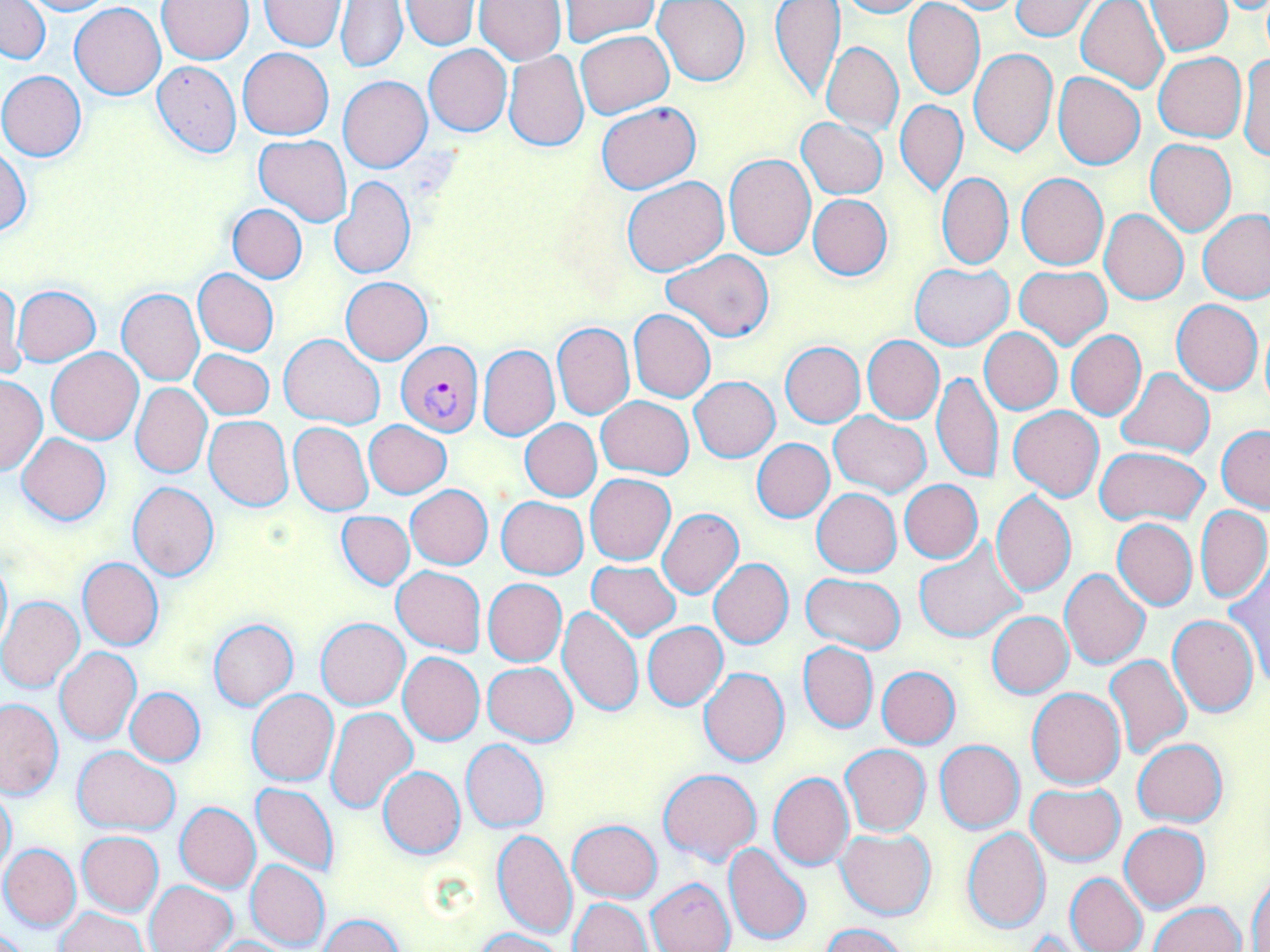
Summary:
  - Coordinate format: approximate bounding boxes as [x1, y1, x2, y2] in pixels
  - Uninfected red blood cell locations: [1, 0, 51, 65], [19, 0, 113, 15], [158, 0, 254, 64], [473, 0, 565, 65], [560, 0, 660, 46], [654, 0, 750, 86], [770, 0, 844, 102], [833, 0, 930, 18], [929, 0, 1028, 15], [1010, 0, 1101, 40], [1145, 0, 1232, 56], [259, 1, 347, 51], [336, 1, 407, 72], [401, 1, 478, 51], [1076, 1, 1168, 95], [904, 2, 985, 101], [70, 3, 166, 100], [575, 30, 673, 116], [821, 43, 903, 135], [423, 45, 511, 136], [238, 47, 334, 138], [968, 47, 1057, 156], [503, 50, 589, 152], [1238, 51, 1270, 161], [1154, 52, 1247, 142], [151, 59, 241, 159], [0, 70, 86, 161], [1053, 72, 1146, 170], [338, 75, 432, 172], [896, 98, 967, 197], [596, 101, 699, 193], [797, 117, 888, 199], [254, 135, 353, 227], [1145, 139, 1236, 236], [0, 147, 30, 237], [723, 154, 815, 260], [937, 172, 1013, 269], [1016, 173, 1108, 269], [622, 176, 730, 276], [331, 177, 415, 280], [807, 194, 892, 280], [227, 204, 307, 283], [1100, 209, 1188, 304], [1199, 211, 1270, 304], [662, 249, 774, 342], [910, 264, 1013, 350], [1013, 266, 1112, 349], [193, 269, 279, 355], [340, 276, 432, 365], [1, 280, 23, 380], [12, 285, 100, 365], [117, 288, 204, 385], [1172, 299, 1263, 395], [628, 308, 715, 402], [1259, 320, 1270, 414], [552, 321, 634, 420], [980, 328, 1062, 414], [1066, 330, 1146, 420], [279, 334, 383, 427], [862, 336, 943, 423], [781, 342, 865, 427], [478, 345, 559, 440], [46, 348, 143, 444], [191, 349, 274, 419], [1116, 368, 1215, 458], [932, 371, 1003, 485], [0, 375, 48, 476], [689, 377, 779, 462], [131, 383, 211, 478], [597, 396, 694, 478], [1008, 405, 1104, 501], [829, 411, 930, 497], [204, 416, 294, 511], [364, 420, 451, 498], [520, 420, 601, 501], [288, 421, 372, 515], [1217, 426, 1270, 512], [17, 432, 111, 525], [751, 438, 835, 523], [1094, 446, 1209, 525], [585, 474, 675, 565], [899, 480, 983, 563], [128, 482, 221, 580], [407, 485, 493, 569], [811, 489, 901, 577], [991, 491, 1076, 597], [497, 496, 588, 578], [1195, 505, 1270, 602], [657, 508, 744, 598], [336, 512, 414, 589], [1112, 519, 1197, 611], [914, 539, 1028, 643], [0, 555, 11, 655], [77, 557, 164, 651], [708, 558, 793, 648], [586, 561, 681, 641], [1225, 564, 1270, 690], [392, 565, 485, 655], [1059, 569, 1151, 671], [800, 573, 906, 654], [483, 578, 567, 666], [0, 596, 84, 692], [555, 603, 643, 717], [986, 611, 1073, 698], [1167, 613, 1259, 717], [316, 618, 409, 709], [208, 619, 299, 710], [643, 622, 729, 710], [797, 641, 877, 733], [55, 647, 141, 744], [398, 651, 484, 745], [1105, 654, 1192, 760], [483, 661, 577, 746], [699, 667, 790, 767], [876, 667, 960, 749], [125, 687, 205, 766], [246, 688, 339, 786], [1026, 688, 1125, 790], [0, 698, 64, 798], [326, 707, 418, 814], [462, 739, 548, 832], [1132, 739, 1227, 826], [934, 740, 1025, 834], [838, 744, 931, 836], [72, 746, 180, 834], [377, 767, 465, 858], [658, 768, 761, 867], [768, 772, 854, 870], [251, 782, 338, 876], [1025, 783, 1124, 865], [0, 784, 16, 878], [175, 802, 260, 892], [749, 803, 837, 926], [568, 819, 662, 901], [1119, 822, 1208, 913], [961, 825, 1051, 933], [493, 829, 576, 940], [836, 829, 937, 920], [76, 831, 164, 917], [723, 843, 812, 947], [1, 844, 81, 930], [246, 860, 330, 949], [1248, 869, 1270, 952], [1065, 873, 1148, 952], [646, 877, 734, 952], [145, 880, 238, 952], [569, 897, 651, 951], [1150, 901, 1245, 952], [56, 907, 146, 952], [319, 913, 404, 952], [819, 923, 912, 952], [0, 927, 34, 952], [471, 928, 568, 952], [204, 936, 297, 952]
  - Plasmodium falciparum-infected red blood cell locations: [395, 341, 484, 436]
  - Slide-level diagnosis: Plasmodium falciparum
  - Modality: light microscopy
  - Field of view: single
  - Stain: May-Grünwald-Giemsa
  - Preparation: thin blood film
  - Image size: 1270×952 pixels
  - Magnification: 1000x